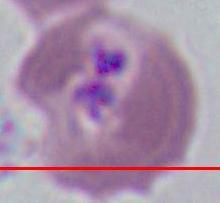

Photomicrograph. A Plasmodium parasite is shown. Captured at either 400x or 1000x magnification.